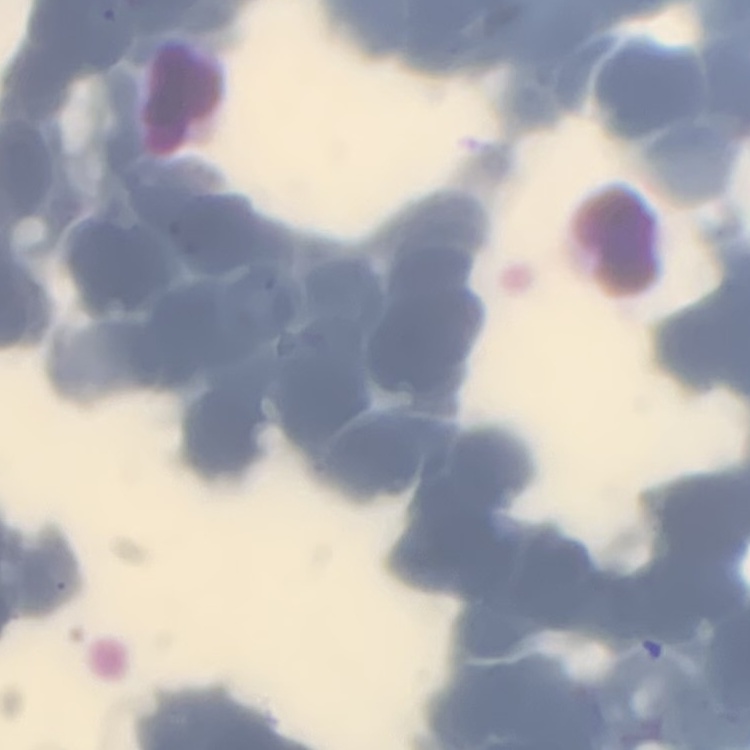
erythrocyte morphology = rouleaux formation
preparation = thin peripheral smear
stain = Field's or Giemsa
image type = one tile cut from a larger photomicrograph